Locate every Trypanosoma brucei.
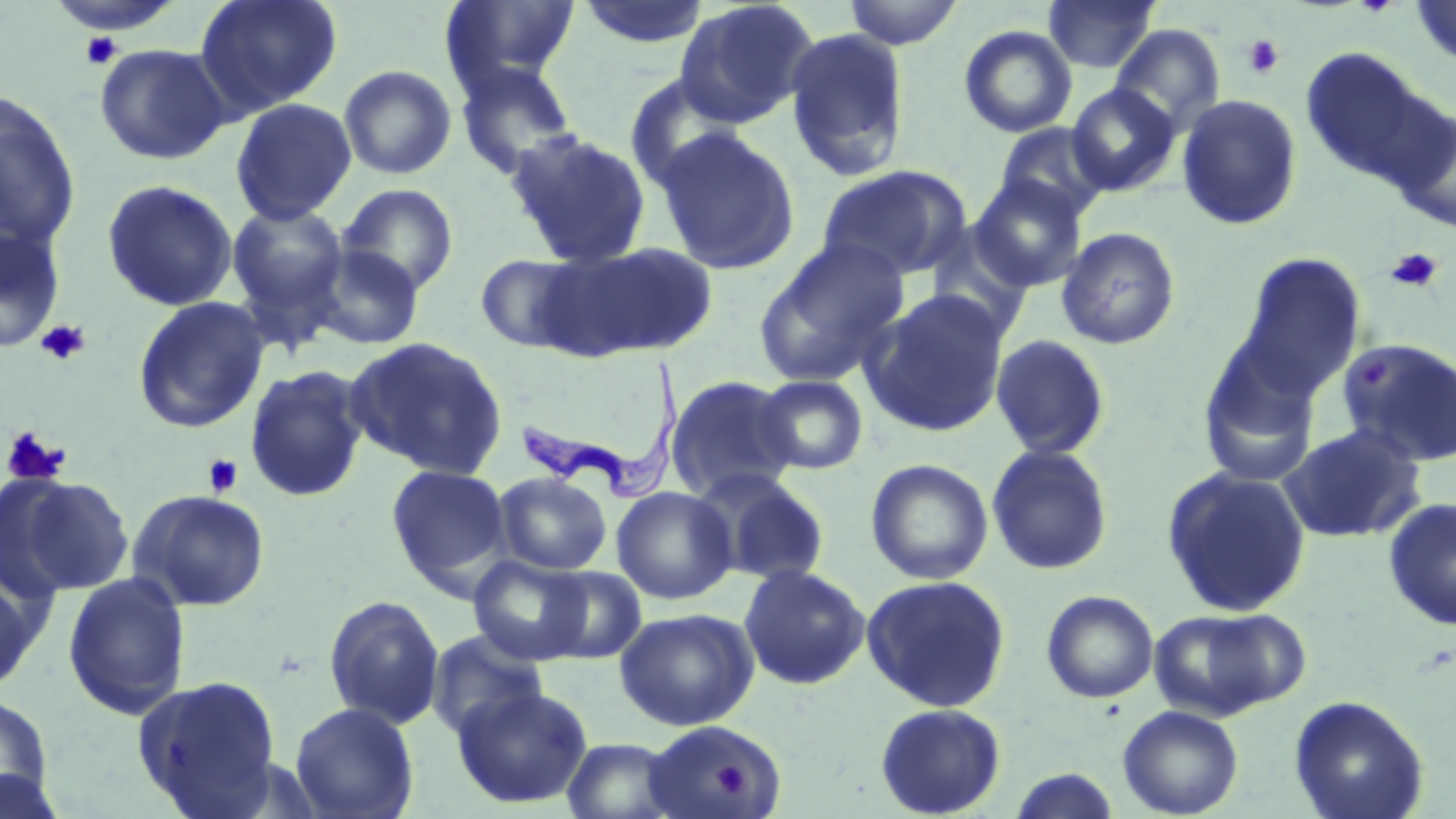
Approximate bounding boxes as [x1, y1, x2, y2] in pixels.
Trypanosoma brucei: [515, 358, 688, 508].

slide-level diagnosis = Trypanosoma brucei
preparation = thin blood smear
field of view = one of a larger specimen
image size = 1456×819 pixels
uninfected red blood cell locations = approximate bounding boxes as [x1, y1, x2, y2] in pixels: [195, 0, 343, 117], [442, 0, 582, 92], [841, 0, 965, 49], [1043, 0, 1160, 74], [1411, 0, 1456, 67], [577, 1, 710, 50], [674, 1, 820, 128], [1110, 23, 1225, 136], [959, 24, 1077, 138], [784, 28, 911, 182], [94, 43, 232, 165], [1299, 47, 1438, 186], [454, 60, 580, 180], [338, 64, 457, 180], [624, 73, 746, 191], [1066, 83, 1180, 196], [0, 92, 82, 252], [1176, 93, 1303, 231], [230, 98, 357, 225], [1389, 106, 1455, 234], [994, 122, 1111, 223], [655, 128, 800, 275], [504, 129, 653, 267], [817, 164, 971, 281], [969, 177, 1088, 292], [101, 179, 238, 311], [337, 183, 459, 296], [225, 201, 351, 329], [0, 224, 65, 353], [1055, 226, 1181, 350], [754, 238, 910, 387], [540, 241, 718, 361], [309, 243, 426, 350], [1234, 252, 1366, 400], [474, 253, 592, 353], [861, 288, 1011, 437], [132, 296, 270, 434], [990, 334, 1111, 460], [345, 336, 509, 480], [1337, 338, 1456, 467], [1196, 339, 1323, 489], [243, 364, 370, 503], [665, 374, 801, 502], [756, 374, 869, 475], [1277, 423, 1427, 545], [986, 444, 1114, 576], [866, 458, 993, 585], [386, 464, 512, 590], [1160, 466, 1312, 618], [694, 470, 832, 586], [493, 471, 612, 575], [5, 474, 135, 596], [611, 486, 737, 605], [128, 488, 271, 612], [1383, 497, 1456, 631], [468, 554, 594, 665], [738, 564, 870, 690], [539, 566, 647, 663], [62, 572, 191, 720], [0, 573, 42, 696], [860, 575, 1012, 712], [1041, 590, 1159, 703], [323, 594, 445, 730], [1148, 605, 1306, 721], [615, 607, 759, 730], [426, 629, 549, 741], [132, 674, 283, 817], [451, 685, 594, 809], [0, 692, 55, 812], [1288, 695, 1429, 819], [289, 702, 419, 819], [874, 702, 1007, 818], [1118, 704, 1243, 818], [641, 721, 782, 819], [560, 737, 684, 819], [1004, 766, 1125, 818], [0, 768, 69, 819]
platelet locations = approximate bounding boxes as [x1, y1, x2, y2] in pixels: [79, 32, 123, 70], [1243, 34, 1285, 79], [1386, 248, 1443, 293], [36, 319, 91, 366], [2, 427, 71, 487], [203, 454, 243, 497], [711, 764, 749, 796]
stain = May-Grünwald-Giemsa
magnification = 1000x
modality = light microscopy